Give the extent of all Plasmodium falciparum-infected red blood cells.
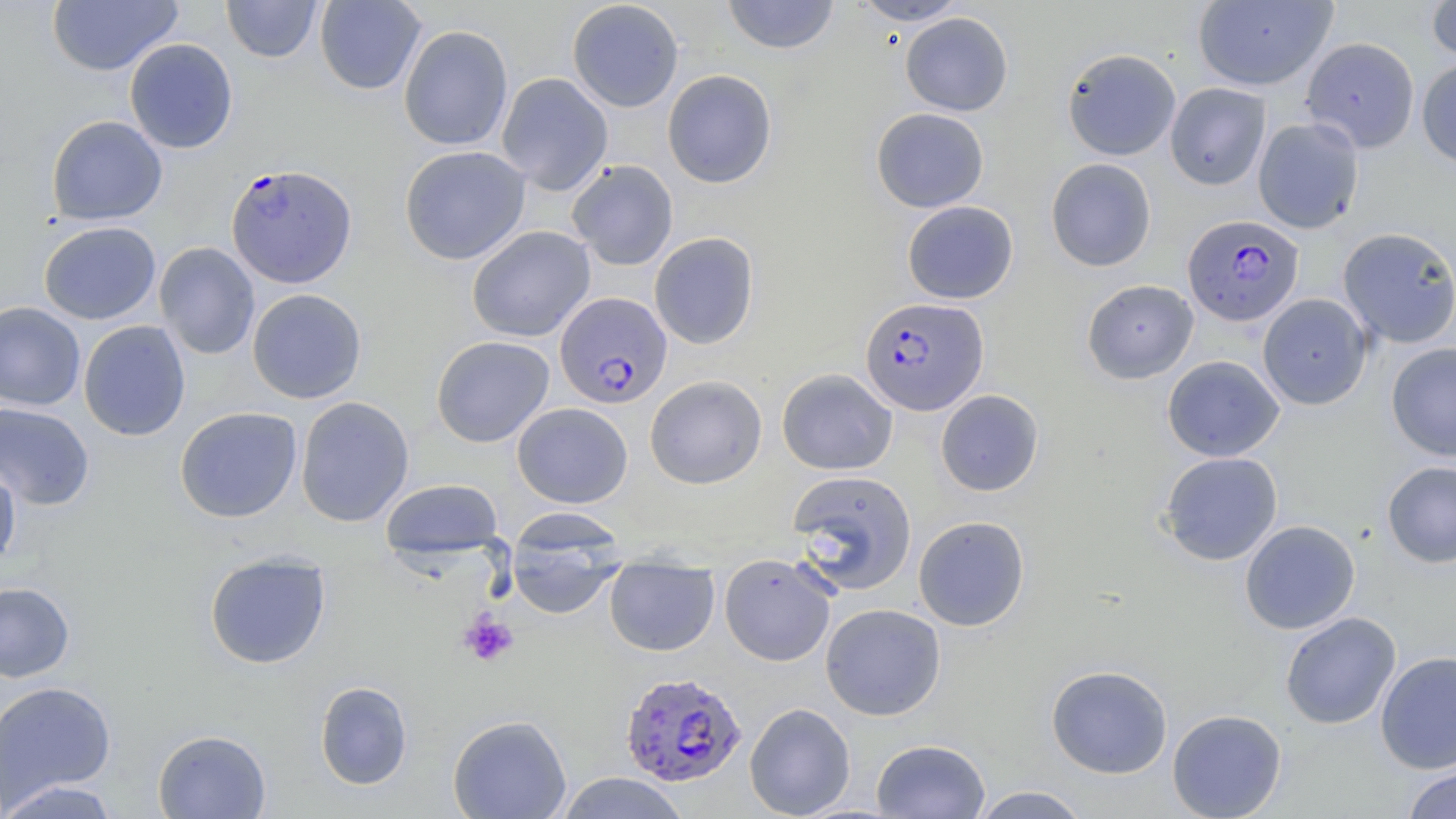

Approximate bounding boxes as (x1, y1, x2, y2) in pixels.
Plasmodium falciparum-infected red blood cells: (226, 163, 357, 287), (1183, 214, 1304, 327), (554, 292, 672, 408), (859, 296, 988, 415), (619, 671, 746, 787).

Platelet locations: (459, 611, 519, 667). Uninfected red blood cell locations: (221, 0, 323, 63), (314, 0, 426, 95), (722, 0, 840, 55), (850, 0, 970, 26), (46, 1, 182, 76), (566, 1, 684, 112), (1193, 1, 1337, 91), (1426, 1, 1456, 64), (900, 12, 1013, 116), (398, 24, 513, 151), (1300, 37, 1420, 152), (124, 38, 238, 154), (1054, 47, 1167, 272), (1062, 48, 1181, 160), (1416, 58, 1456, 169), (662, 69, 777, 188), (496, 72, 613, 195), (1164, 82, 1271, 190), (871, 107, 989, 213), (46, 115, 167, 225), (1253, 117, 1364, 234), (399, 145, 530, 265), (1045, 157, 1157, 271), (567, 159, 679, 271), (902, 201, 1018, 304), (38, 221, 161, 325), (467, 226, 595, 342), (1337, 226, 1456, 348), (649, 232, 759, 349), (154, 242, 260, 360), (1081, 279, 1199, 384), (247, 288, 367, 404), (1258, 293, 1372, 410), (0, 302, 86, 411), (78, 320, 191, 441), (431, 336, 555, 447), (1386, 341, 1456, 462), (1162, 355, 1285, 461), (777, 368, 898, 475), (644, 375, 767, 489), (935, 389, 1044, 496), (295, 396, 415, 527), (0, 402, 95, 510), (512, 402, 633, 508), (175, 406, 302, 523), (1158, 451, 1283, 566), (0, 460, 21, 571), (1381, 461, 1456, 568), (786, 469, 918, 594), (380, 478, 504, 561), (913, 515, 1030, 631), (506, 520, 626, 620), (1239, 520, 1361, 634), (203, 551, 331, 669), (719, 553, 837, 666), (604, 559, 720, 657), (0, 581, 75, 683), (820, 603, 946, 721), (1280, 612, 1401, 730), (1375, 651, 1456, 774), (1046, 664, 1173, 778), (0, 680, 117, 809), (314, 681, 413, 790), (744, 702, 856, 818), (1167, 708, 1287, 818), (447, 713, 572, 819), (152, 729, 271, 818), (871, 738, 990, 818), (1401, 764, 1456, 819), (554, 772, 691, 818), (1, 779, 124, 818), (970, 785, 1092, 818). Slide-level diagnosis: Plasmodium falciparum. One field of a larger specimen. Thin blood smear. Optical microscopy. Captured at 1000x magnification. Image is 1456×819 pixels. May-Grünwald-Giemsa-stained preparation.